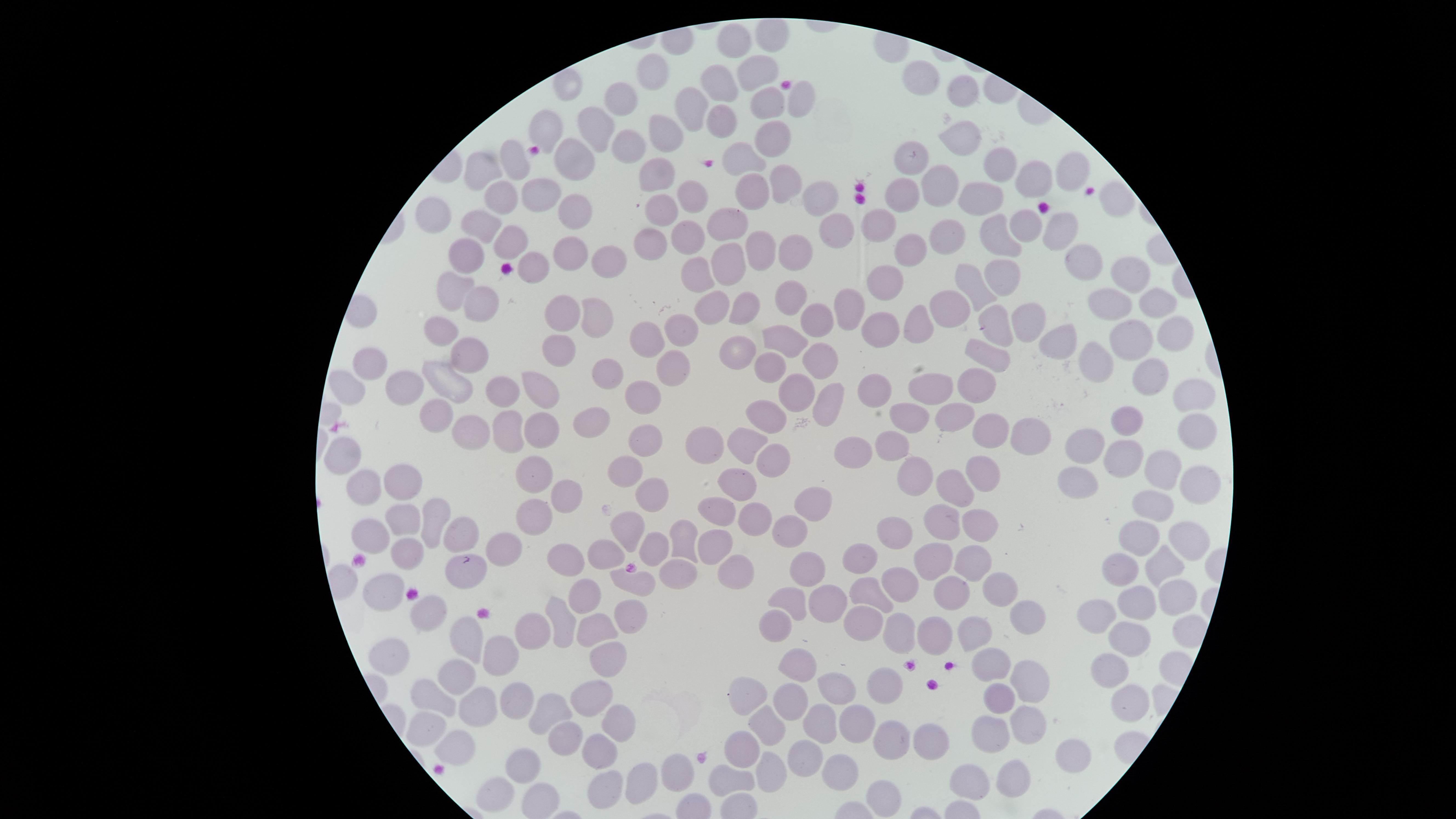 Approximate marker points as [x, y] in pixels. Uninfected red blood cells: [773, 41], [734, 43], [751, 71], [655, 74], [925, 78], [724, 83], [568, 87], [963, 92], [619, 97], [800, 101], [692, 105], [764, 105], [720, 122], [546, 126], [597, 128], [668, 133], [770, 139], [622, 141], [964, 141], [575, 157], [513, 160], [745, 160], [914, 160], [998, 165], [485, 168], [1067, 169], [659, 171], [1037, 177], [786, 180], [940, 182], [547, 191], [752, 191], [499, 195], [904, 195], [690, 196], [820, 198], [981, 199], [1116, 202], [660, 206], [574, 213], [440, 217], [732, 219], [481, 224], [1024, 224], [878, 226], [1062, 226], [832, 233], [693, 238], [998, 238], [950, 239], [511, 240], [651, 247], [761, 248], [908, 249], [571, 250], [459, 251], [796, 253], [1084, 258], [615, 260], [728, 260], [536, 263], [702, 268], [1005, 274], [1125, 274], [888, 283], [459, 284], [969, 285], [790, 294], [1152, 299], [483, 300], [1101, 301], [708, 306], [852, 307], [743, 309], [948, 309], [565, 313], [596, 318], [817, 319], [923, 321], [1025, 322], [999, 323], [879, 325], [684, 328], [438, 329], [1177, 329], [783, 337], [652, 339], [1123, 339], [1060, 340], [558, 348], [734, 350], [472, 354], [1098, 355], [993, 358], [818, 361], [668, 364], [765, 365], [369, 368], [607, 370], [1148, 373], [976, 382], [451, 385], [543, 385], [404, 386], [509, 388], [1188, 390], [344, 391], [790, 391], [876, 391], [928, 394], [646, 398], [827, 403], [435, 414], [769, 416], [951, 417], [587, 419], [912, 420], [1126, 420], [507, 428], [1195, 428], [537, 429], [985, 432], [469, 433], [1026, 434], [644, 438], [703, 439], [886, 445], [1083, 445], [346, 452], [856, 452], [1125, 456], [773, 462], [1161, 463], [982, 468], [537, 469], [623, 471], [1076, 482], [403, 483], [915, 483], [741, 484], [368, 486], [1197, 488], [953, 492], [569, 498], [657, 501], [1152, 502], [721, 503], [812, 509], [757, 512], [534, 517], [401, 519], [434, 522], [944, 522], [982, 524], [790, 529], [379, 532], [629, 533], [468, 535], [895, 536], [1137, 537], [1191, 540], [677, 542], [713, 543], [650, 544], [511, 549], [607, 554], [932, 555], [404, 556], [963, 559], [865, 560], [1160, 560], [567, 562], [462, 566], [1129, 567], [813, 568], [732, 570], [677, 572], [907, 579], [639, 580], [382, 585], [950, 585], [997, 585], [864, 590], [1178, 593], [832, 596], [792, 599], [585, 600], [1139, 605], [431, 613], [1105, 614], [631, 620], [773, 620], [859, 620], [565, 623], [1031, 624], [590, 629], [533, 632], [893, 632], [932, 634], [1134, 634], [972, 635], [472, 638], [391, 654], [506, 660], [991, 661], [611, 663], [802, 666], [1112, 674], [456, 679], [1033, 679], [880, 688], [838, 689], [748, 693], [514, 695], [592, 695], [434, 697], [1129, 697], [1001, 702], [792, 704], [475, 706], [551, 710], [851, 724], [1026, 724], [620, 726], [427, 728], [823, 729], [769, 733], [987, 739], [928, 741], [891, 742], [567, 743], [458, 748], [747, 749], [602, 751], [1085, 754], [812, 757], [840, 764], [521, 771], [679, 772], [769, 773], [1008, 775], [646, 779], [733, 783], [962, 783], [605, 785], [497, 798], [535, 798], [884, 799]. Giemsa-stained preparation. Image is 1456×819 pixels. Presence: no malaria parasites identified. Circular visible region. One field of view of the specimen. Smartphone photograph through the microscope eyepiece. Thin blood smear.